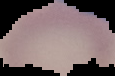

From a thin blood film. Image is 115×76 pixels. Result: no malaria parasites detected. The area outside the segmented cell region is set to black.